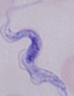
Summary:
  - Identification: trypanosome
  - Modality: micrograph
  - Magnification: 1000x